Identify the parasite.
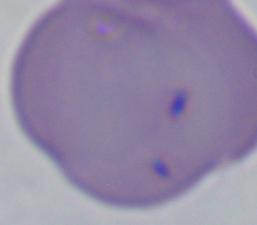
This is Babesia.

magnification: 1000x
modality: photomicrograph